Describe the morphology of the red blood cells.
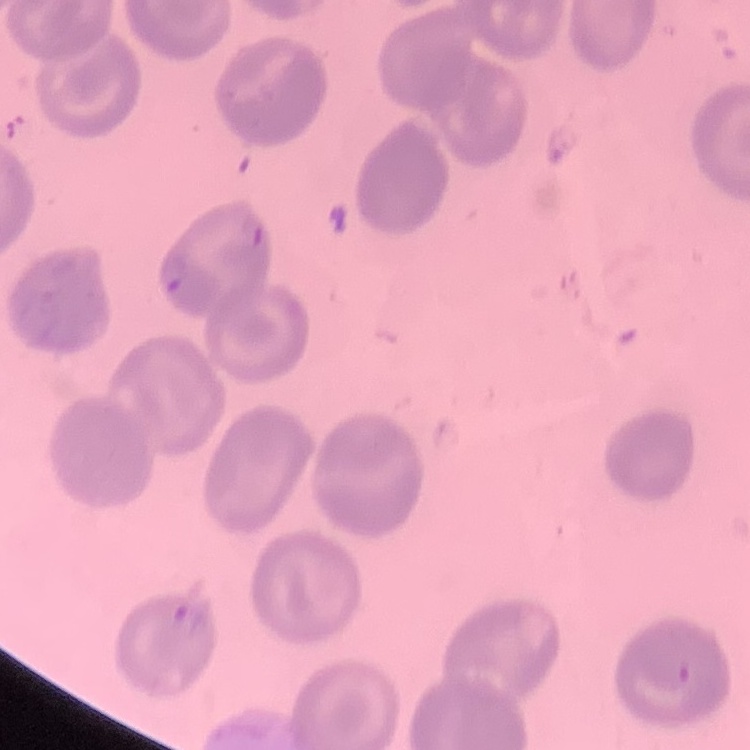

They show no rouleaux formation.

Summary:
  - Preparation: thin blood film
  - Stain: Field's or Giemsa
  - Image type: square crop of a larger photomicrograph